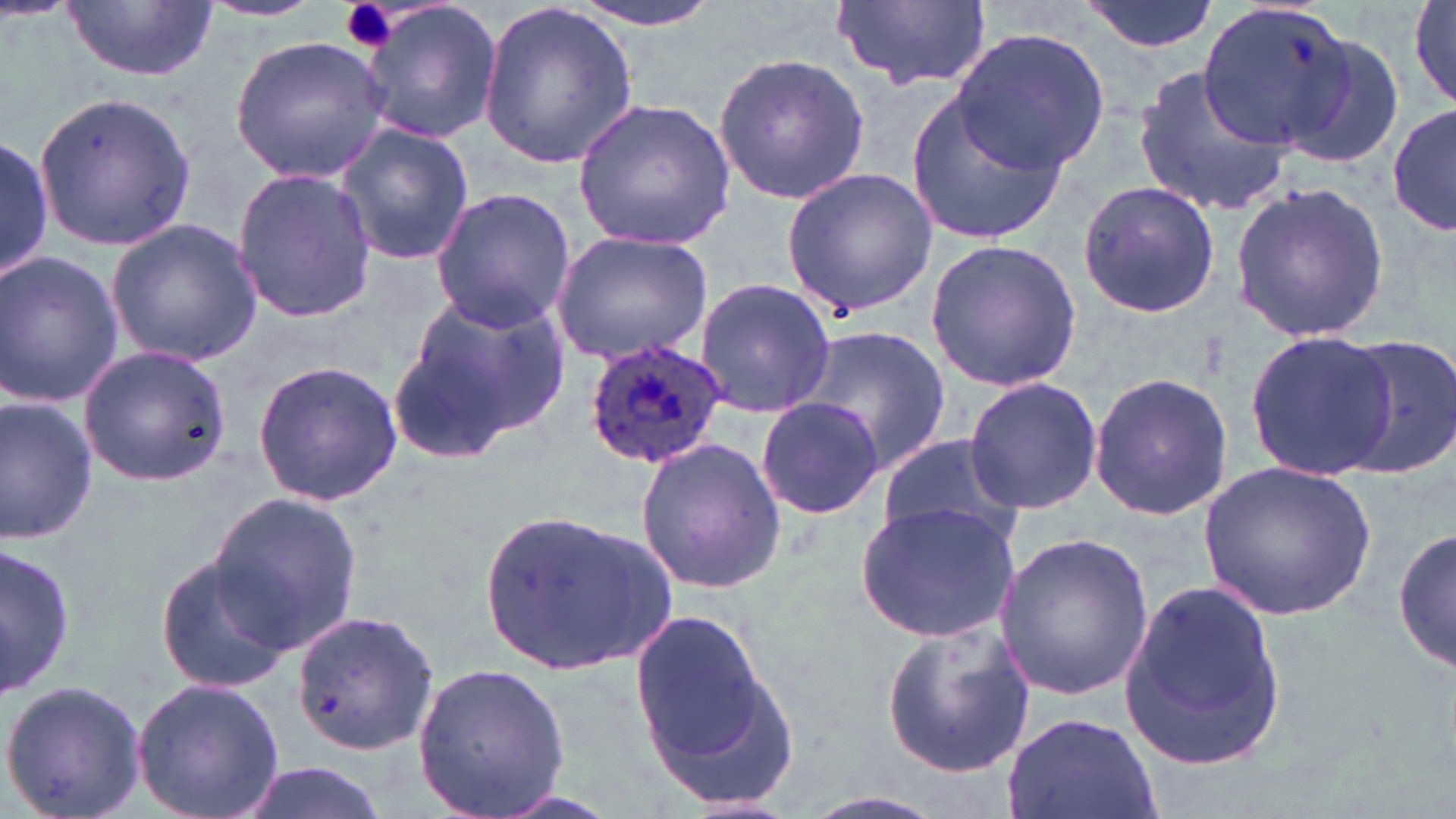
slide-level diagnosis = Plasmodium ovale
uninfected red blood cell locations = approximate bounding boxes as named x1/y1/x2/y2 corners in pixels: (x1=62, y1=0, x2=218, y2=83), (x1=359, y1=0, x2=500, y2=144), (x1=477, y1=0, x2=637, y2=170), (x1=559, y1=0, x2=729, y2=32), (x1=829, y1=0, x2=991, y2=93), (x1=1080, y1=0, x2=1217, y2=53), (x1=1406, y1=0, x2=1456, y2=113), (x1=199, y1=1, x2=329, y2=22), (x1=1199, y1=3, x2=1379, y2=154), (x1=951, y1=28, x2=1108, y2=176), (x1=1283, y1=31, x2=1407, y2=168), (x1=229, y1=37, x2=392, y2=182), (x1=712, y1=51, x2=868, y2=204), (x1=1132, y1=65, x2=1293, y2=218), (x1=905, y1=89, x2=1072, y2=247), (x1=33, y1=90, x2=195, y2=250), (x1=571, y1=95, x2=738, y2=252), (x1=1388, y1=103, x2=1454, y2=239), (x1=334, y1=122, x2=478, y2=267), (x1=0, y1=132, x2=54, y2=288), (x1=780, y1=168, x2=937, y2=316), (x1=230, y1=169, x2=376, y2=322), (x1=1077, y1=178, x2=1220, y2=321), (x1=1227, y1=182, x2=1391, y2=342), (x1=428, y1=186, x2=577, y2=332), (x1=105, y1=219, x2=265, y2=367), (x1=549, y1=230, x2=715, y2=364), (x1=924, y1=239, x2=1082, y2=391), (x1=0, y1=250, x2=124, y2=406), (x1=693, y1=277, x2=837, y2=418), (x1=398, y1=288, x2=571, y2=448), (x1=800, y1=326, x2=950, y2=477), (x1=1246, y1=329, x2=1398, y2=478), (x1=1340, y1=335, x2=1456, y2=480), (x1=77, y1=344, x2=230, y2=486), (x1=252, y1=359, x2=404, y2=507), (x1=1088, y1=371, x2=1235, y2=522), (x1=964, y1=377, x2=1103, y2=514), (x1=0, y1=394, x2=100, y2=545), (x1=755, y1=396, x2=884, y2=522), (x1=877, y1=435, x2=1026, y2=552), (x1=633, y1=437, x2=786, y2=593), (x1=1199, y1=459, x2=1377, y2=622), (x1=207, y1=493, x2=364, y2=651), (x1=857, y1=502, x2=1023, y2=642), (x1=477, y1=509, x2=671, y2=675), (x1=1393, y1=521, x2=1455, y2=679), (x1=992, y1=531, x2=1153, y2=700), (x1=0, y1=540, x2=76, y2=703), (x1=154, y1=553, x2=297, y2=693), (x1=1117, y1=573, x2=1287, y2=774), (x1=626, y1=606, x2=788, y2=792), (x1=289, y1=609, x2=440, y2=754), (x1=879, y1=621, x2=1036, y2=775), (x1=410, y1=659, x2=571, y2=816), (x1=130, y1=677, x2=284, y2=819), (x1=0, y1=678, x2=147, y2=819), (x1=1000, y1=714, x2=1162, y2=819), (x1=230, y1=761, x2=394, y2=819), (x1=790, y1=791, x2=953, y2=819)
preparation = thin blood smear
modality = optical microscopy
stain = May-Grünwald-Giemsa
platelet locations = approximate bounding boxes as named x1/y1/x2/y2 corners in pixels: (x1=337, y1=0, x2=398, y2=55)
field of view = single
magnification = 1000x
image size = 1456×819 pixels
Plasmodium ovale-infected red blood cell locations = approximate bounding boxes as named x1/y1/x2/y2 corners in pixels: (x1=580, y1=338, x2=729, y2=472)